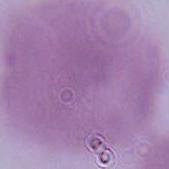

identification: red blood cell
modality: micrograph
magnification: 1000x